Assess this cell for malaria.
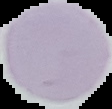

It is uninfected.

{
  "preparation": "thin blood film",
  "image_size": "112×109 pixels",
  "image_type": "cell region segmented out of the field of view; surrounding area masked to black"
}